Point out malaria parasites and leukocytes.
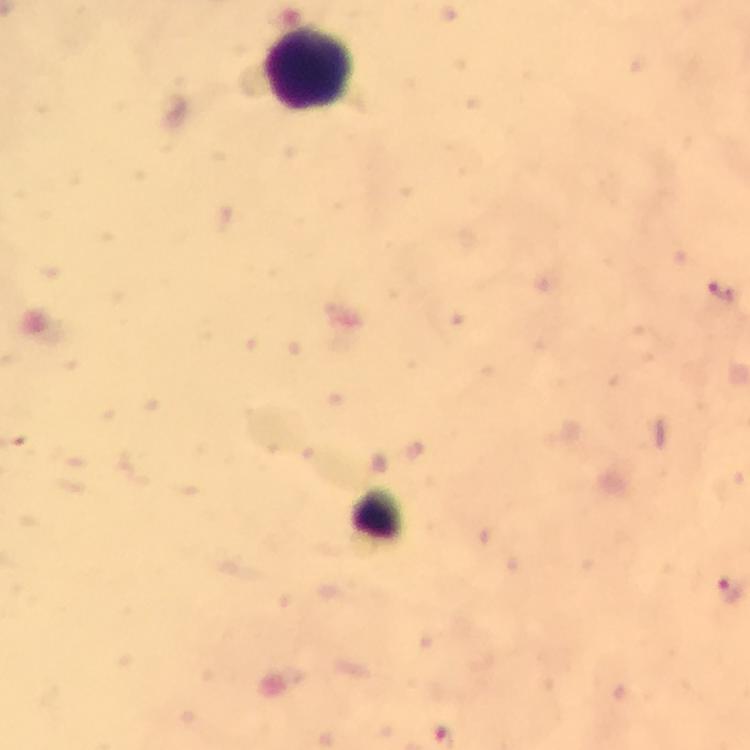
No malaria parasites detected.
Approximate centers as {x, y} in pixels.
Leukocytes: {307, 68}.

{
  "context": "from a diagnostic examination for malaria",
  "immersion_oil": "applied",
  "capture": "smartphone mounted on the microscope",
  "image_size": "750×750 pixels",
  "preparation": "thick blood film",
  "magnification": "100x",
  "cropped_from": "a single field of view",
  "stain": "Giemsa"
}